Give the preparation type.
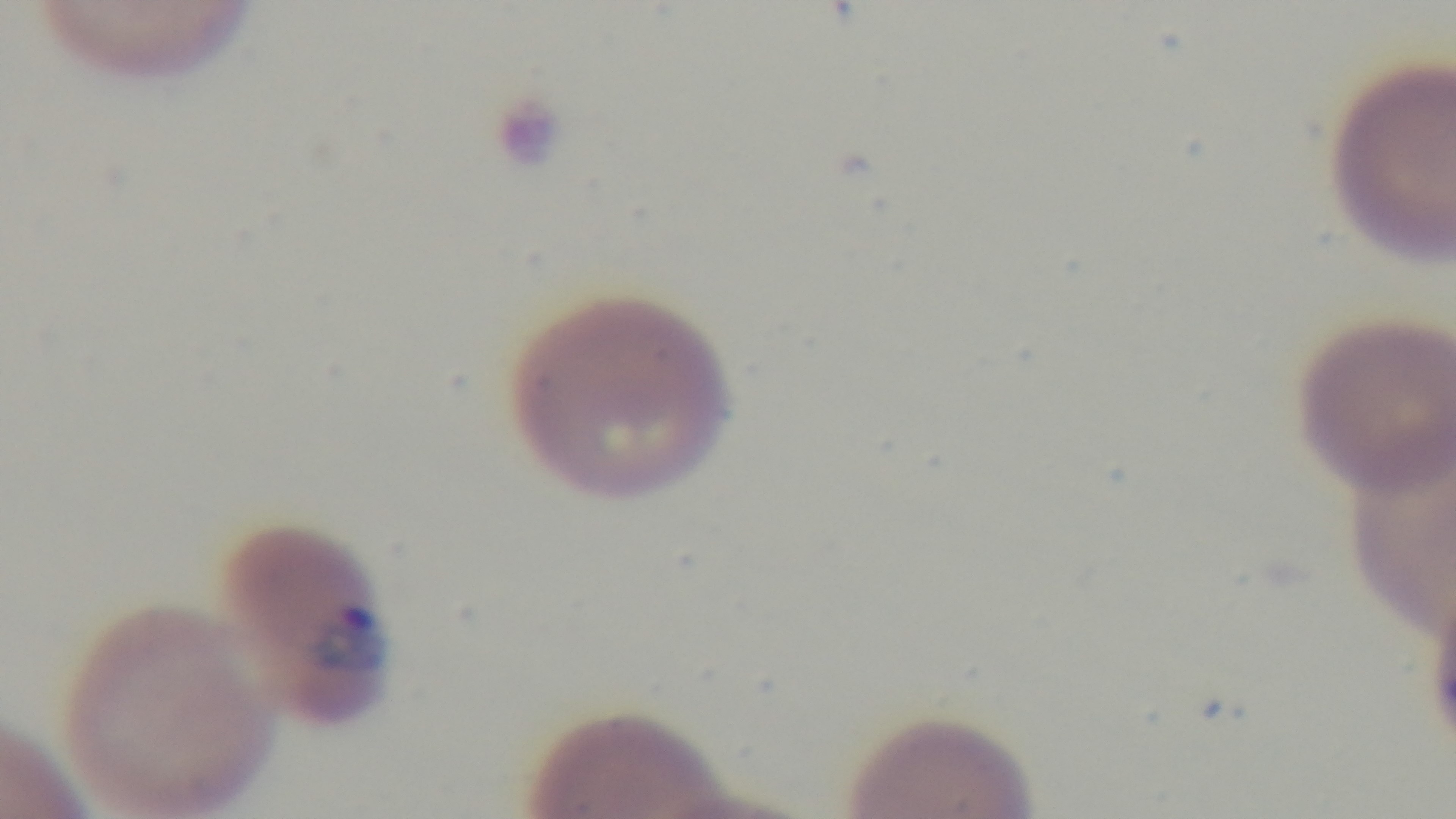

It is a thin blood film.

Summary:
  - Modality: light microscopy
  - Stain: Giemsa
  - Capture: mounted 4K digital camera
  - Field of view: single
  - Malaria status: positive
  - Objective: 100x oil immersion